State the blood parasite species.
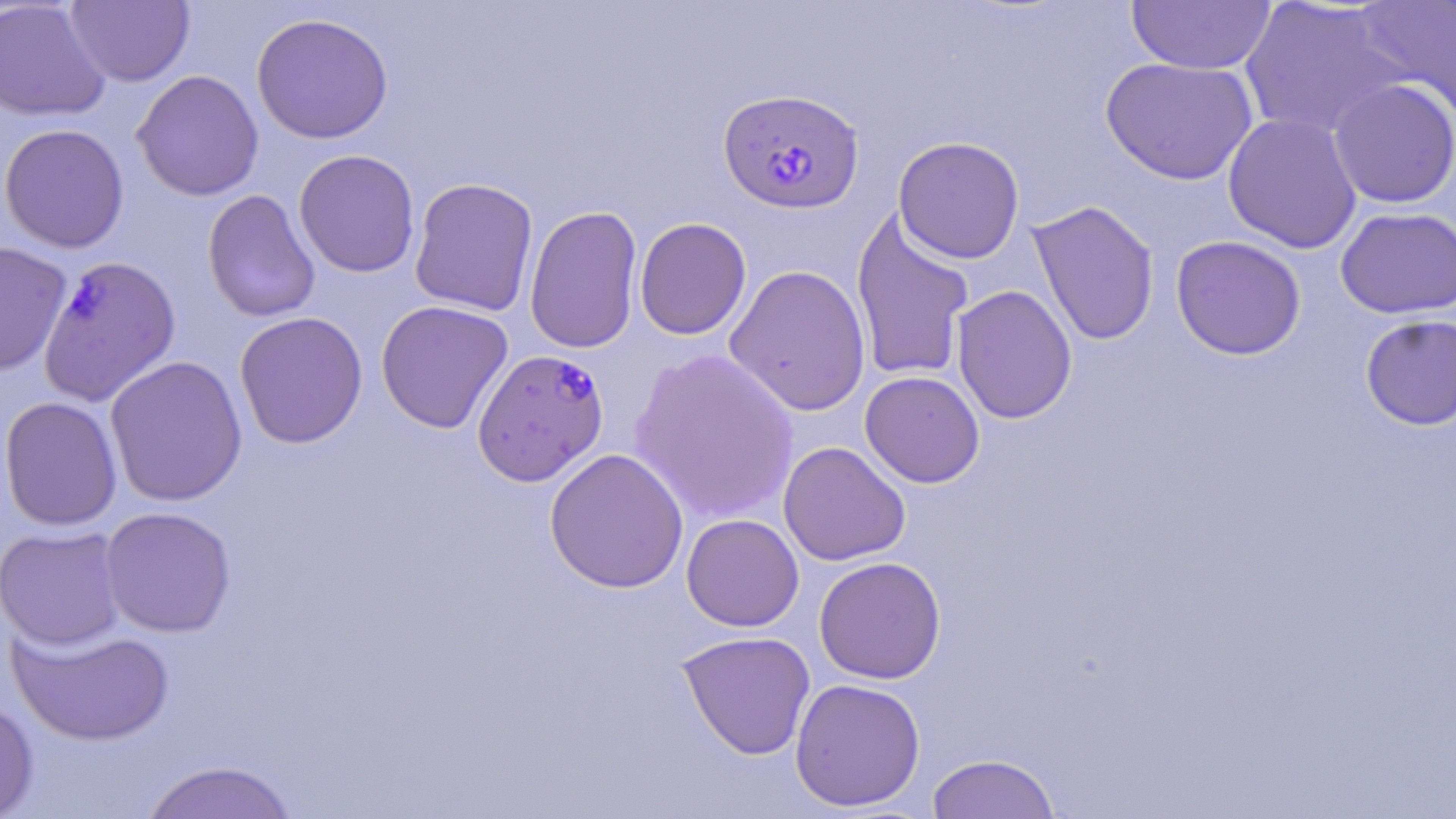
Plasmodium falciparum.

Approximate bounding boxes as (x1, y1, x2, y2) in pixels. Plasmodium falciparum-infected red blood cell locations: (718, 87, 866, 214), (38, 254, 182, 406), (472, 349, 609, 486). Uninfected red blood cell locations: (0, 0, 110, 121), (65, 0, 195, 87), (1354, 0, 1456, 120), (1126, 1, 1276, 75), (1238, 1, 1411, 140), (251, 12, 394, 144), (1100, 57, 1258, 184), (131, 69, 265, 201), (1328, 78, 1456, 208), (1222, 112, 1362, 253), (0, 123, 129, 253), (893, 136, 1026, 263), (294, 149, 420, 277), (409, 177, 539, 316), (202, 189, 321, 323), (1028, 199, 1161, 346), (524, 205, 643, 354), (1335, 206, 1456, 318), (851, 210, 975, 384), (634, 217, 752, 340), (1170, 235, 1306, 360), (0, 240, 72, 377), (724, 264, 871, 417), (952, 285, 1077, 424), (375, 299, 514, 433), (233, 311, 369, 449), (1360, 314, 1456, 430), (629, 348, 799, 523), (104, 355, 248, 507), (860, 371, 985, 488), (0, 396, 123, 531), (778, 441, 911, 566), (544, 448, 690, 593), (99, 506, 237, 637), (681, 513, 804, 632), (1, 526, 127, 650), (814, 556, 946, 684), (7, 622, 175, 746), (677, 631, 816, 759), (789, 678, 926, 811), (0, 696, 39, 819), (926, 753, 1061, 818), (139, 759, 301, 819). Captured at 1000x magnification. One field of a larger specimen. May-Grünwald-Giemsa-stained preparation. Light microscopy. Image is 1456×819 pixels. Thin blood film.